Report the malaria status of this cell.
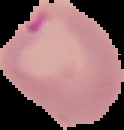
It is parasitized.

From a thin blood smear. Segmented cell region on a black background. Image is 124×130 pixels.